Give the position of every Plasmodium parasite.
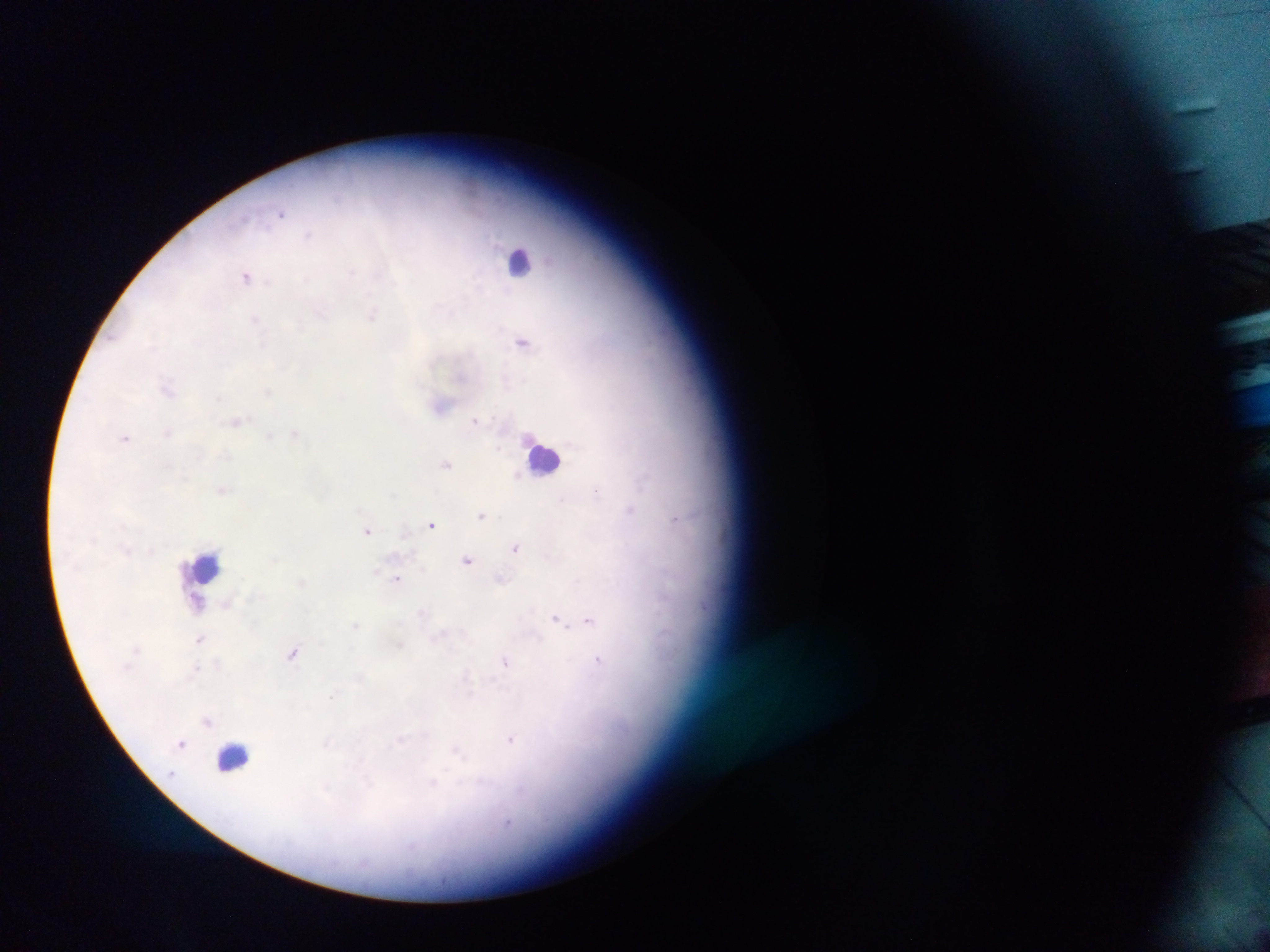

Approximate centers as x y in pixels.
Plasmodium parasites: 281 214; 308 234; 350 273; 246 276; 307 279; 321 313; 372 314; 256 318; 300 324; 522 341; 262 344; 168 389; 268 392; 218 398; 475 420; 237 422; 167 433; 295 434; 269 436; 125 438; 226 455; 199 456; 446 463; 518 474; 644 478; 222 490; 596 490; 562 500; 630 510; 482 515; 675 519; 432 524; 368 530; 516 547; 467 560; 500 578; 397 579; 301 582; 227 604; 422 613; 557 619; 588 620; 356 624; 200 639; 400 646; 293 652; 506 662; 598 662; 195 670; 467 679; 332 696; 208 721; 511 739; 181 743; 326 744; 456 751; 171 774; 433 784.

Summary:
  - Leukocyte locations: 519 260; 544 457; 206 567; 199 603; 234 758
  - Capture: mobile-phone photograph through a microscope
  - Preparation: thick blood film
  - Field of view: single
  - Country: Ghana
  - Image size: 1270×952 pixels